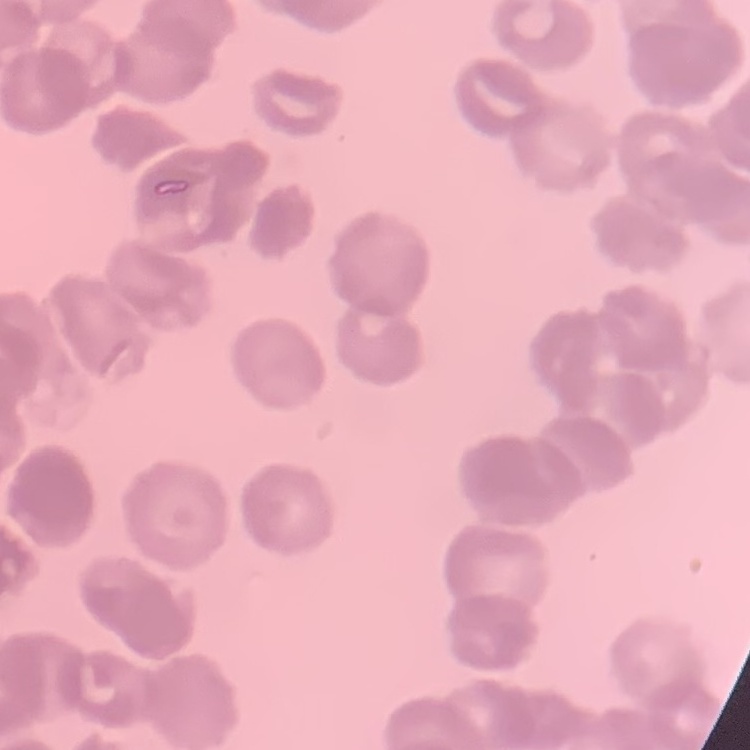

The red blood cells show rouleaux formation. Stained with either Field's or Giemsa. One tile cut from a larger photomicrograph. Thin blood smear.